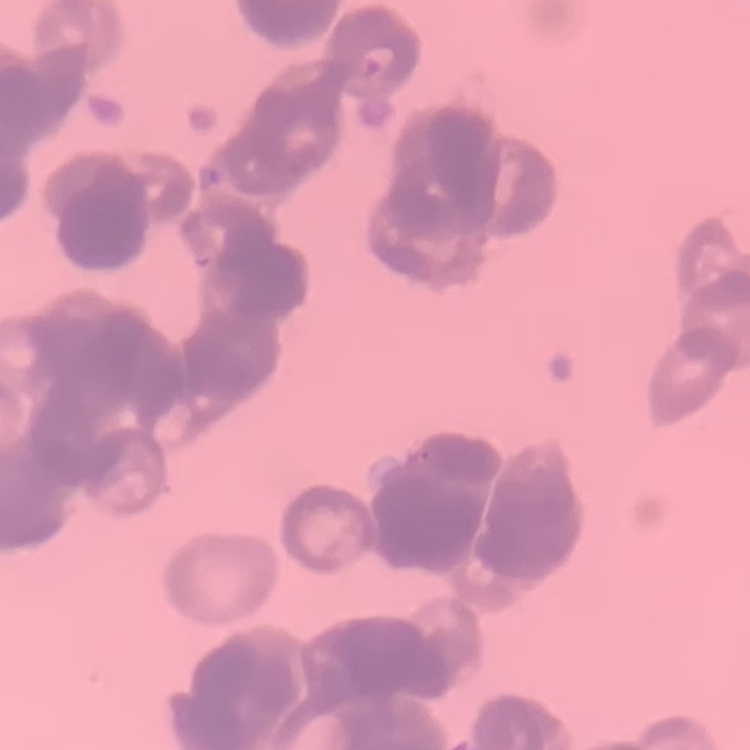

The erythrocytes show rouleaux formation. Field's or Giemsa stain. Square crop of a larger photomicrograph. Thin peripheral smear.